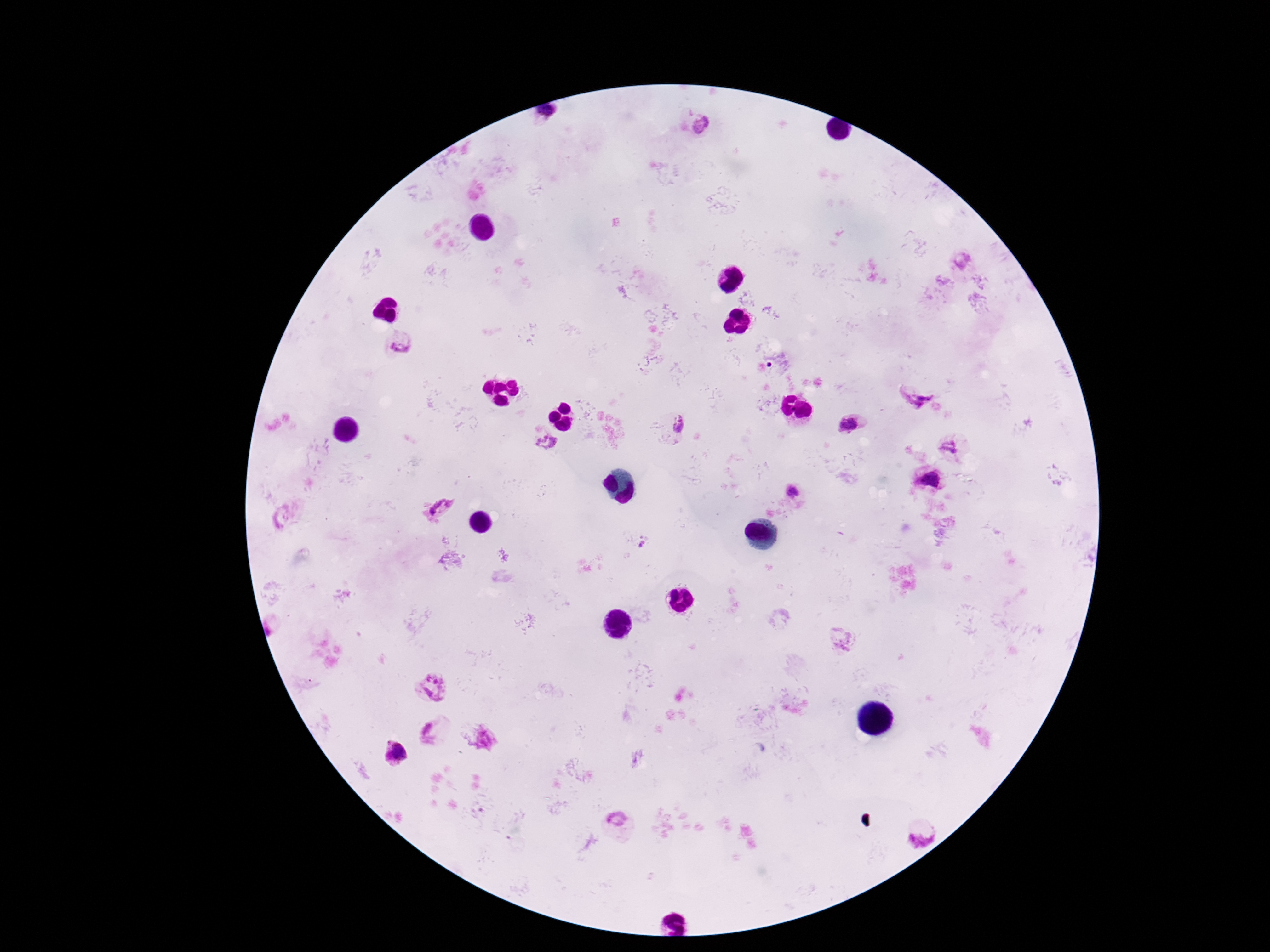
patient_malaria_status: positive
plasmodium_parasite_locations: 'approximate centers as (x, y) in pixels: (546, 115), (704, 124), (963, 258), (402, 343), (916, 391), (680, 423), (848, 423), (546, 441), (950, 447), (930, 479), (794, 490), (441, 508), (842, 637), (434, 686), (429, 729), (393, 752), (617, 818), (922, 831)'
magnification: 100x
preparation: thick blood smear
image_size: 1270×952 pixels
stain: Giemsa
field_of_view: single
capture: smartphone camera through the microscope eyepiece